Point out each Plasmodium parasite.
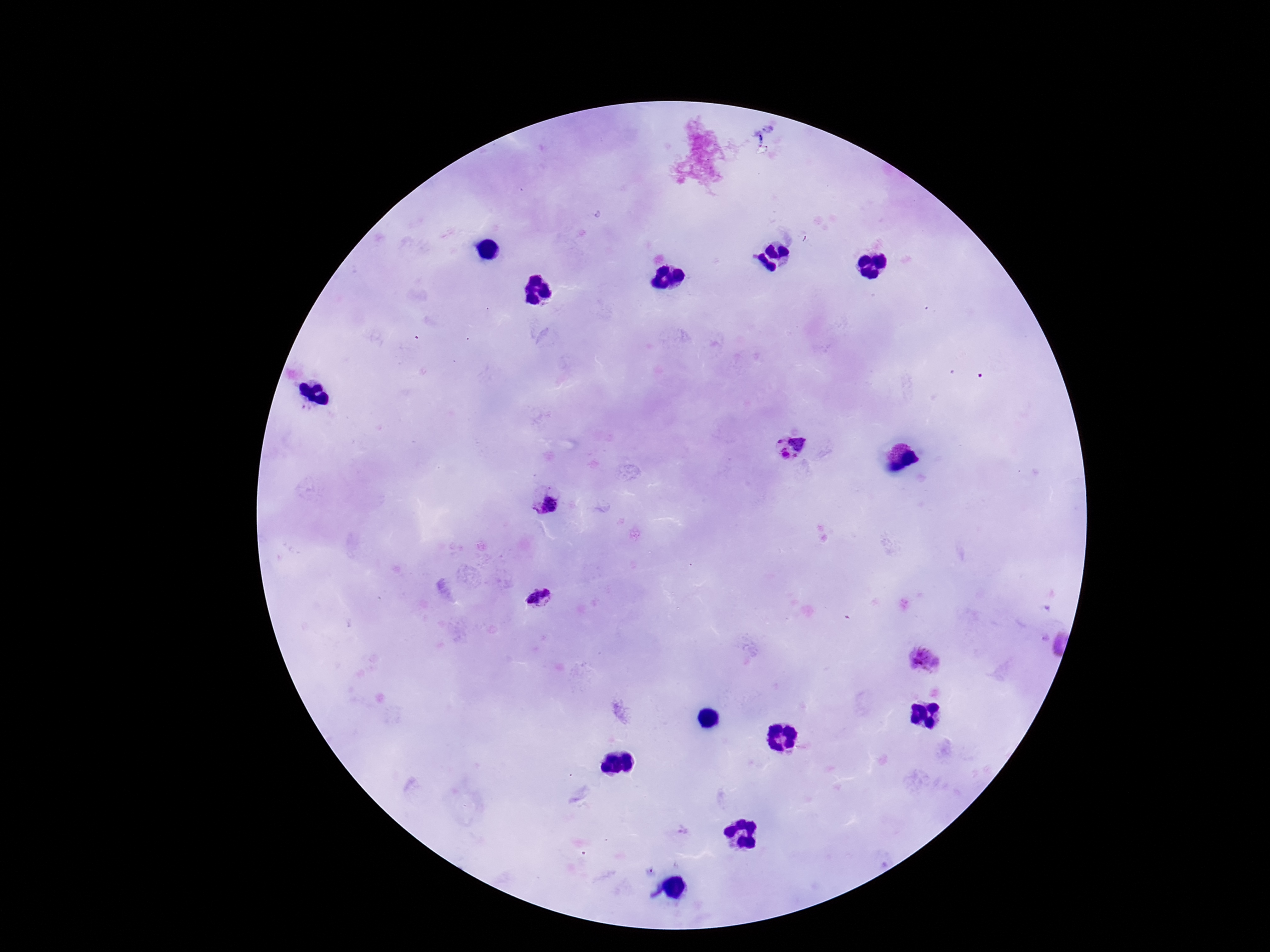
Approximate centers as (x, y) in pixels.
Plasmodium parasites: (791, 447), (545, 501), (538, 599), (925, 660).

Summary:
  - Image size: 1270×952 pixels
  - Preparation: thick peripheral-blood smear
  - Field of view: single
  - Magnification: 100x
  - Stain: Giemsa
  - Capture: smartphone camera through the microscope eyepiece
  - Patient malaria status: positive